Report the malaria status of this cell.
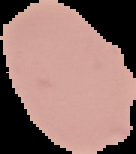

It is uninfected.

Summary:
  - Image type: segmented cell region on a black background
  - Image size: 136×154 pixels
  - Preparation: thin blood film